Assess this cell for malaria.
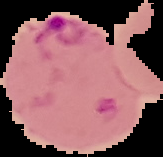

Parasitized.

From a thin blood film. Cell region segmented out of the field of view; the surrounding area is masked to black. Image is 163×157 pixels.